Assess the morphology of the erythrocytes.
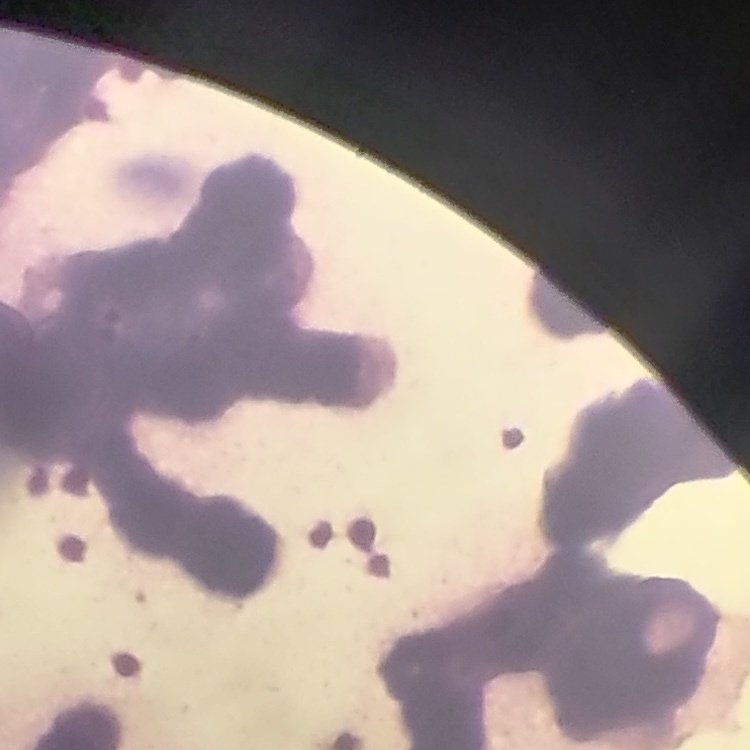

They show rouleaux formation.

Stained with either Field's or Giemsa. Thin peripheral smear. One tile cut from a larger photomicrograph.